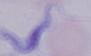
modality = micrograph
identification = trypanosome
magnification = 1000x